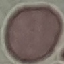
Malaria status: uninfected. Automatically extracted cell patch, resized to 64 × 64 pixels. Giemsa-stained preparation. Photographed with a smartphone camera at the microscope eyepiece. Thin blood smear.